Name the blood parasite species.
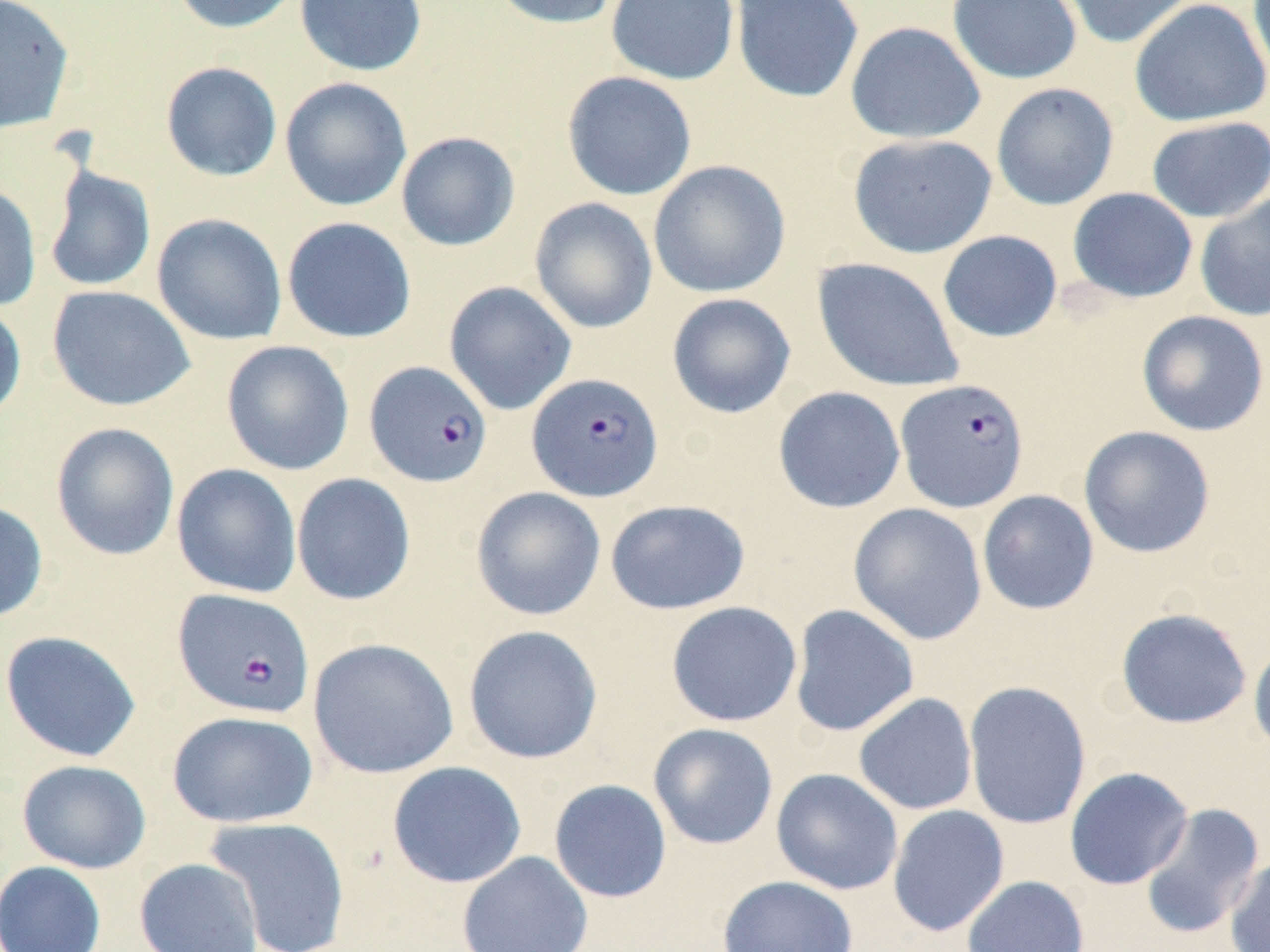

Plasmodium falciparum.

Summary:
  - Coordinate format: approximate bounding boxes as (x1, y1, x2, y2) in pixels
  - Plasmodium falciparum-infected red blood cell locations: (364, 360, 493, 487), (527, 372, 664, 502), (895, 378, 1030, 513), (172, 588, 316, 719)
  - Uninfected red blood cell locations: (0, 0, 75, 134), (168, 0, 304, 35), (294, 0, 428, 76), (486, 0, 625, 30), (605, 0, 740, 85), (730, 0, 864, 104), (947, 0, 1082, 84), (1055, 0, 1197, 49), (1129, 0, 1270, 127), (1247, 0, 1270, 84), (844, 21, 986, 145), (159, 61, 283, 182), (562, 71, 698, 201), (279, 76, 413, 212), (990, 82, 1120, 210), (1146, 116, 1270, 223), (395, 131, 521, 252), (847, 133, 998, 258), (648, 160, 791, 298), (43, 165, 156, 293), (0, 182, 42, 312), (1067, 187, 1198, 303), (1194, 193, 1270, 322), (528, 197, 658, 334), (152, 213, 287, 345), (281, 216, 417, 343), (937, 230, 1063, 342), (812, 257, 965, 392), (443, 281, 577, 415), (46, 285, 196, 411), (667, 293, 797, 419), (0, 299, 27, 425), (1136, 310, 1269, 437), (221, 340, 355, 476), (772, 386, 906, 514), (50, 422, 180, 561), (1078, 425, 1216, 558), (171, 463, 302, 599), (291, 472, 416, 606), (471, 487, 606, 621), (977, 489, 1099, 615), (605, 499, 751, 614), (0, 500, 49, 624), (848, 503, 987, 645), (666, 601, 802, 727), (789, 604, 920, 737), (1115, 607, 1252, 729), (462, 624, 604, 764), (0, 629, 142, 763), (307, 637, 459, 779), (1248, 638, 1270, 758), (963, 681, 1092, 830), (853, 692, 978, 815), (167, 710, 319, 828), (648, 722, 779, 850), (17, 759, 151, 873), (386, 761, 527, 888), (1064, 767, 1194, 890), (771, 768, 903, 895), (548, 779, 672, 903), (1138, 802, 1265, 938), (887, 805, 1010, 937), (205, 816, 351, 952), (457, 850, 594, 952), (1223, 854, 1270, 952), (134, 858, 264, 952), (0, 860, 106, 952), (717, 875, 859, 952), (962, 875, 1090, 952)
  - Field of view: one of a larger specimen
  - Modality: optical microscopy
  - Magnification: 1000x
  - Image size: 1270×952 pixels
  - Preparation: thin blood film
  - Stain: May-Grünwald-Giemsa